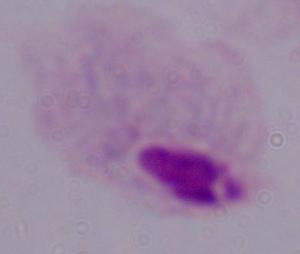

A trichomonad is shown. 1000x magnification. Micrograph.